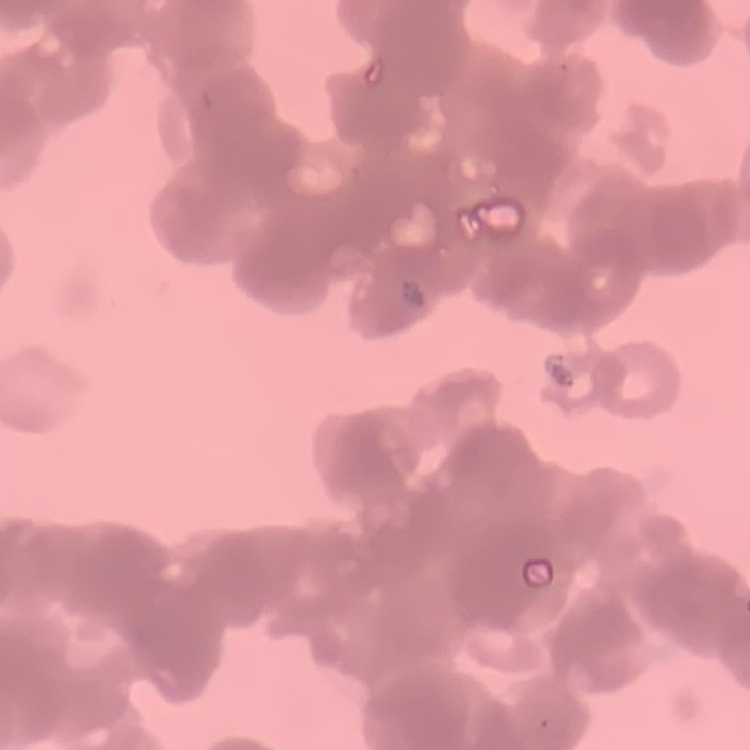
erythrocyte_morphology: rouleaux formation
image_type: one tile cut from a larger photomicrograph
preparation: thin blood smear
stain: Field's or Giemsa